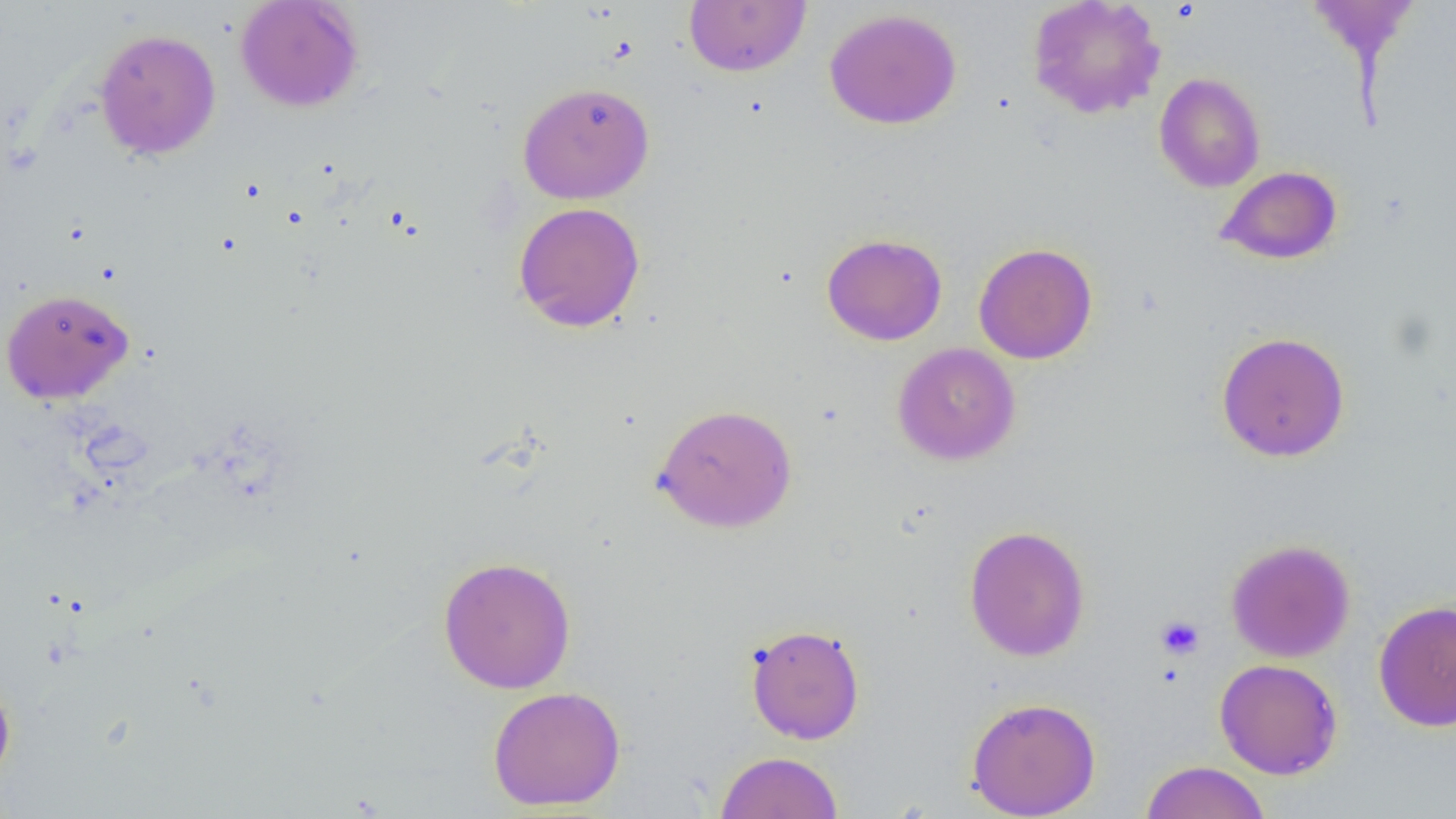
Summary:
  - Coordinate format: approximate bounding boxes as (x1, y1, x2, y2) in pixels
  - Uninfected red blood cell locations: (235, 0, 364, 112), (684, 0, 811, 77), (1026, 0, 1166, 119), (1306, 0, 1419, 66), (824, 8, 962, 129), (93, 28, 222, 160), (1154, 72, 1266, 192), (517, 81, 655, 204), (1216, 165, 1343, 265), (513, 202, 646, 332), (821, 233, 948, 346), (973, 242, 1098, 364), (0, 288, 134, 404), (1215, 331, 1351, 462), (892, 342, 1021, 465), (651, 403, 798, 533), (963, 525, 1091, 661), (1225, 538, 1356, 663), (437, 555, 576, 693), (1373, 598, 1456, 732), (745, 624, 865, 744), (1214, 658, 1343, 780), (0, 673, 16, 787), (487, 685, 626, 811), (966, 696, 1102, 818), (716, 751, 843, 819), (1140, 760, 1271, 819)
  - Platelet locations: (1155, 615, 1205, 660)
  - Slide-level diagnosis: negative for blood parasites
  - Image size: 1456×819 pixels
  - Preparation: thin blood film
  - Field of view: single
  - Magnification: 1000x
  - Modality: optical microscopy